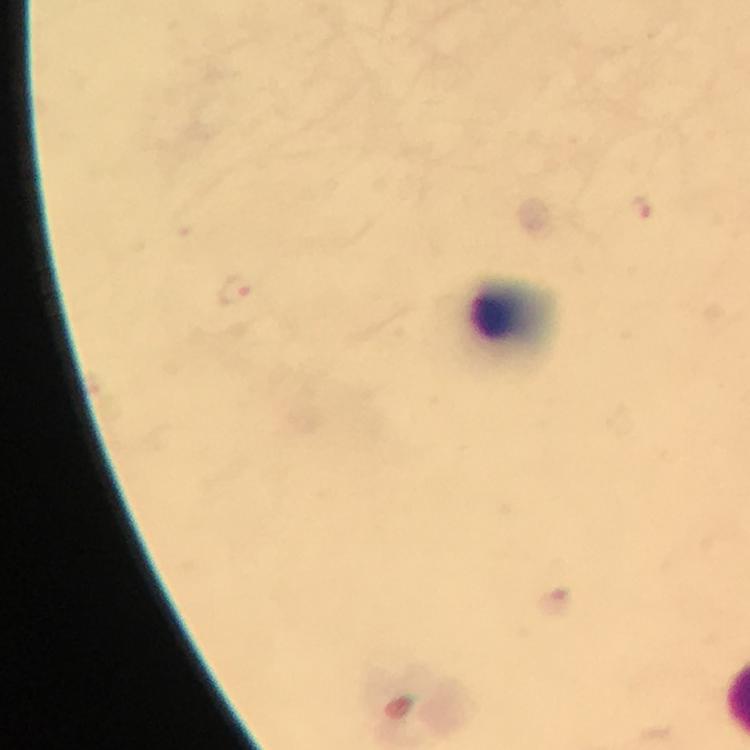

immersion_oil: used
malaria_parasites: none seen
preparation: thick blood film
cropped_from: a single field of view
magnification: 100x
context: from a diagnostic examination for malaria
image_size: 750×750 pixels
capture: smartphone photograph through a microscope
leukocyte_locations: 'approximate object centers, in pixels from the top-left corner: (x=513, y=319)'
stain: Giemsa